Classify this cell by malaria status.
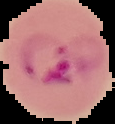
It is parasitized.

Image is 115×124 pixels. The area outside the segmented cell region is set to black. From a thin blood film.